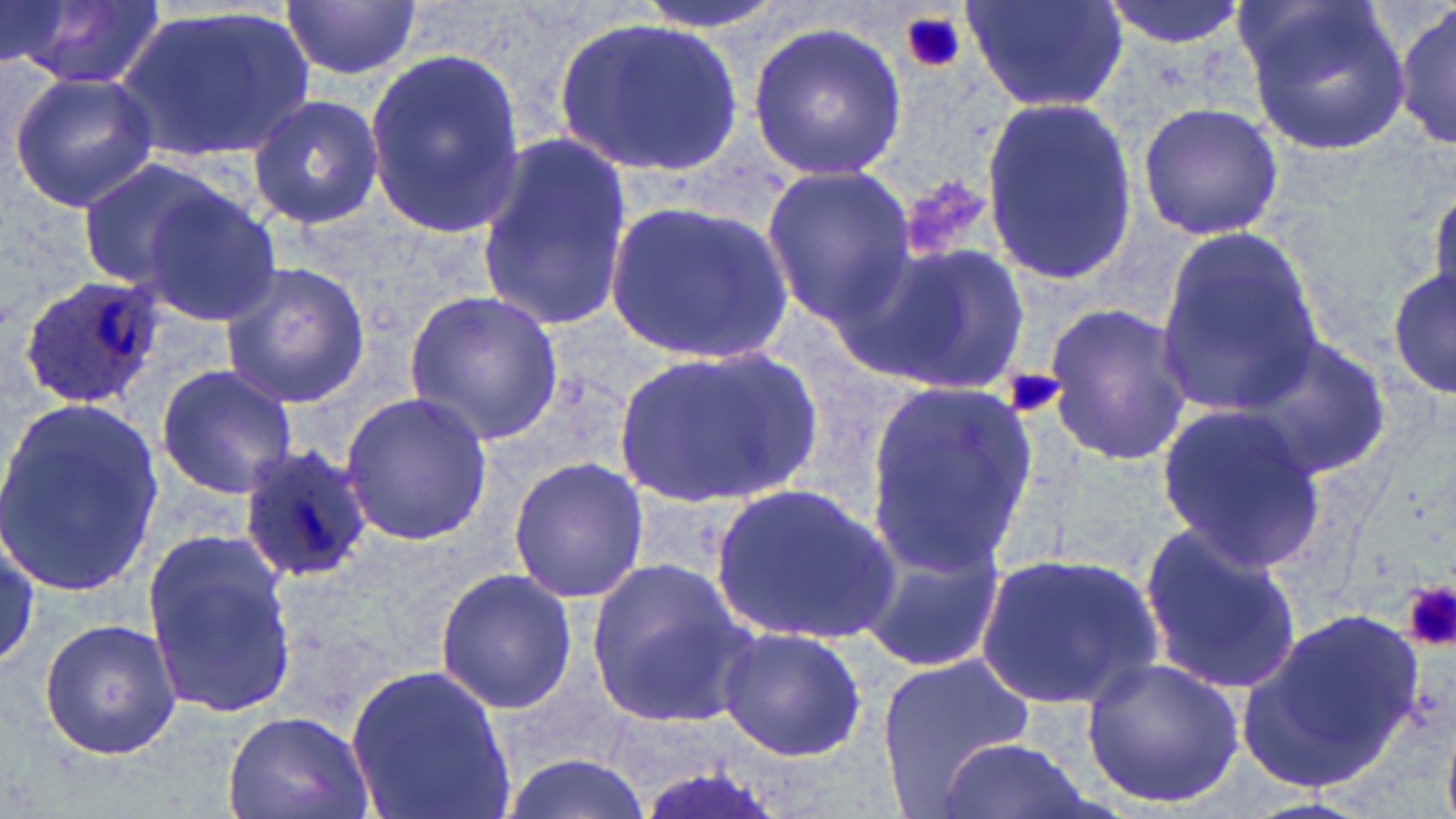

Approximate bounding boxes as [x1, y1, x2, y2] in pixels. Plasmodium ovale-infected red blood cell locations: [15, 274, 164, 409], [239, 443, 376, 581]. Uninfected red blood cell locations: [629, 0, 798, 34], [960, 0, 1129, 114], [1098, 0, 1250, 49], [14, 1, 166, 89], [283, 1, 419, 80], [1243, 1, 1411, 160], [1392, 3, 1455, 151], [116, 4, 315, 164], [555, 15, 743, 180], [746, 21, 908, 183], [363, 48, 524, 234], [8, 71, 159, 212], [978, 93, 1141, 288], [247, 94, 385, 230], [1135, 100, 1285, 241], [473, 132, 632, 332], [75, 155, 233, 292], [761, 166, 916, 324], [1429, 181, 1456, 309], [132, 185, 283, 329], [605, 197, 796, 363], [1157, 230, 1322, 418], [849, 239, 1032, 395], [219, 261, 374, 407], [1388, 268, 1454, 400], [404, 289, 564, 446], [1042, 303, 1192, 470], [1241, 335, 1395, 481], [613, 343, 818, 507], [154, 365, 300, 501], [866, 382, 1040, 571], [338, 391, 492, 547], [0, 399, 163, 596], [1155, 400, 1328, 571], [506, 456, 650, 605], [710, 479, 902, 646], [1137, 520, 1304, 697], [858, 523, 1011, 674], [141, 529, 297, 716], [0, 535, 43, 671], [974, 548, 1168, 711], [583, 556, 755, 731], [433, 567, 578, 713], [1237, 606, 1433, 792], [38, 617, 183, 761], [716, 625, 867, 763], [877, 652, 1036, 807], [1082, 656, 1248, 811], [344, 660, 518, 819], [223, 708, 375, 819], [933, 734, 1094, 819], [497, 751, 649, 819]. Platelet locations: [897, 9, 967, 75], [1004, 367, 1064, 421], [1403, 581, 1456, 652]. Slide-level diagnosis: Plasmodium ovale. Light microscopy. 1000x magnification. Thin blood film. May-Grünwald-Giemsa-stained preparation. Image is 1456×819 pixels. Single field of view.